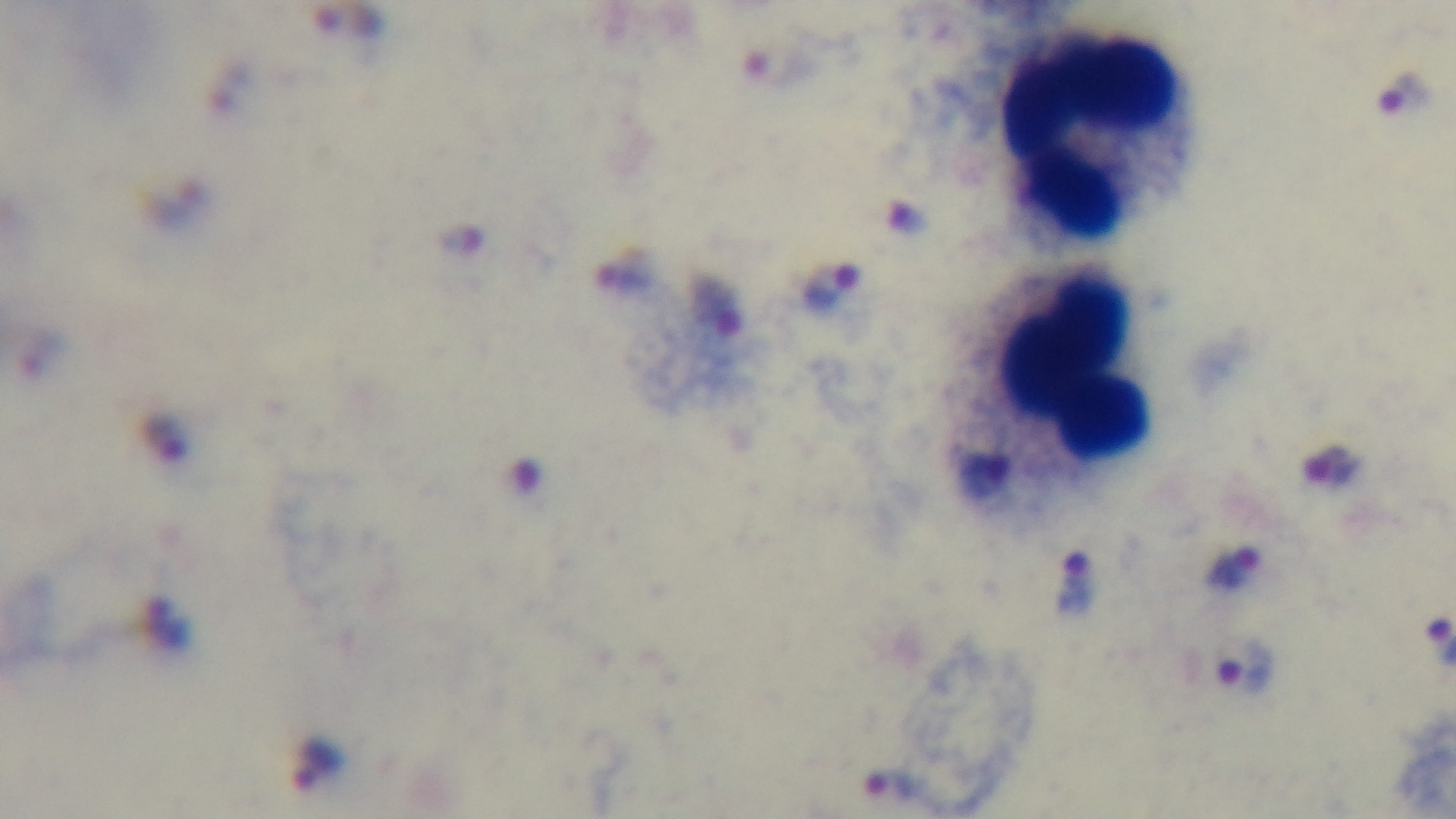

Summary:
  - Preparation: thick smear
  - Malaria status: positive
  - Modality: light microscopy
  - Capture: mounted 4K digital camera
  - Field of view: single
  - Stain: Giemsa
  - Objective: 100x oil immersion